Point out each leukocyte.
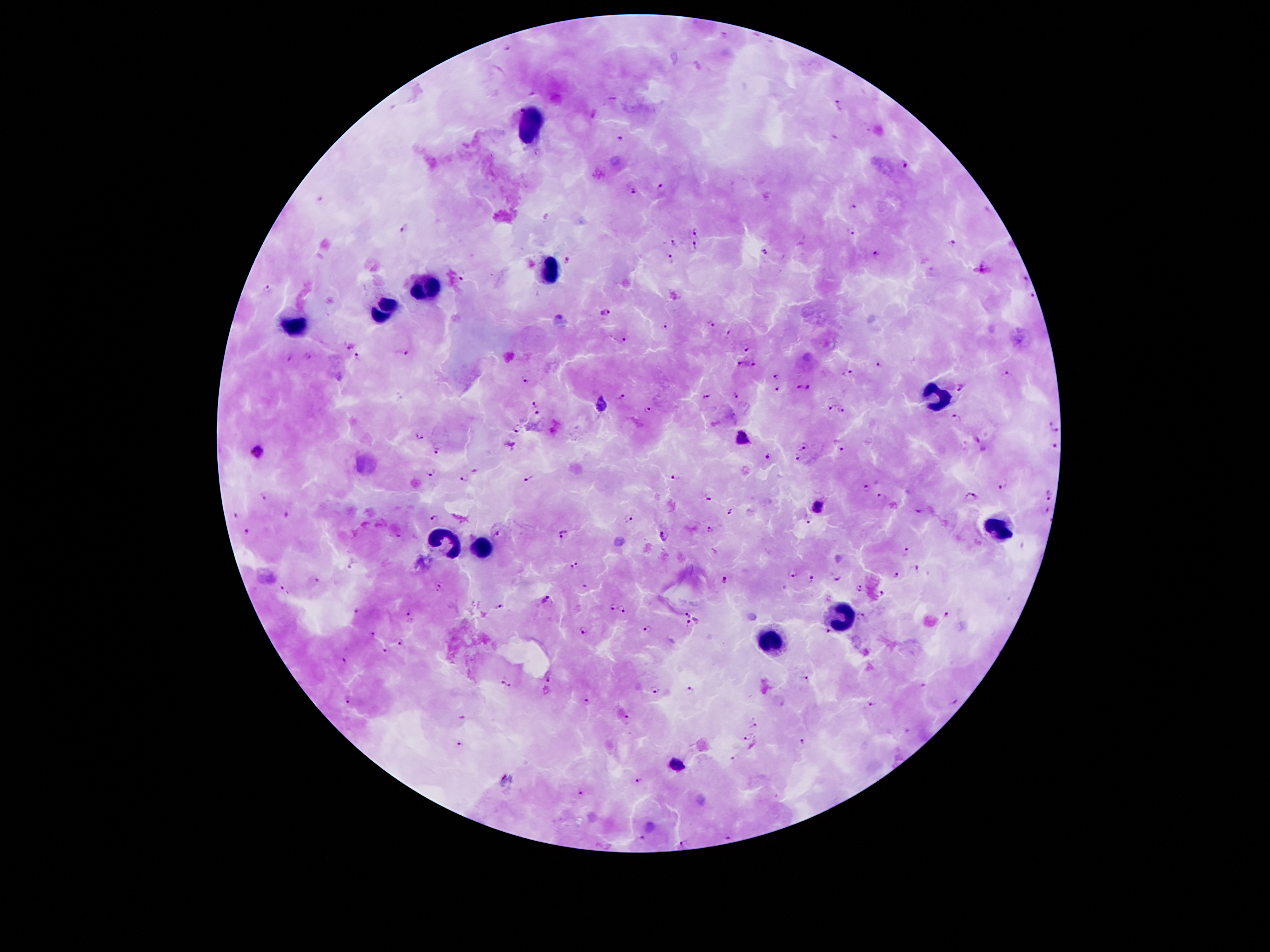

Approximate centers as (x, y) in pixels.
Leukocytes: (528, 120), (547, 269), (428, 286), (385, 309), (293, 327), (938, 394), (1001, 530), (447, 543), (483, 547), (842, 617), (771, 643).

Summary:
  - Malaria parasite locations: (722, 36), (504, 46), (532, 93), (840, 105), (518, 109), (594, 113), (621, 137), (905, 164), (658, 185), (632, 190), (321, 199), (854, 208), (406, 228), (697, 232), (851, 234), (671, 243), (950, 243), (694, 244), (764, 254), (876, 255), (669, 258), (568, 261), (982, 268), (463, 279), (1025, 280), (266, 288), (1030, 295), (603, 313), (711, 324), (667, 328), (730, 332), (623, 339), (346, 343), (747, 347), (404, 353), (289, 356), (358, 357), (304, 358), (741, 363), (879, 364), (753, 365), (847, 373), (1007, 375), (776, 377), (527, 378), (960, 386), (777, 387), (798, 387), (809, 387), (735, 396), (622, 397), (707, 398), (534, 402), (602, 406), (829, 406), (646, 407), (843, 410), (537, 411), (957, 416), (1050, 422), (517, 430), (1055, 431), (420, 437), (978, 438), (741, 440), (965, 444), (806, 445), (509, 447), (842, 447), (1054, 447), (437, 451), (260, 454), (767, 456), (798, 458), (476, 470), (430, 472), (528, 479), (462, 480), (675, 480), (1002, 484), (867, 488), (1049, 495), (263, 496), (880, 496), (970, 497), (706, 499), (819, 508), (919, 510), (1043, 510), (730, 511), (234, 514), (287, 514), (627, 516), (434, 518), (809, 520), (707, 529), (245, 530), (495, 533), (562, 534), (664, 535), (905, 551), (574, 565), (351, 567), (916, 568), (792, 575), (836, 575), (896, 575), (812, 576), (319, 578), (725, 579), (584, 585), (438, 589), (860, 589), (286, 590), (883, 594), (544, 600), (611, 605), (500, 606), (623, 607), (355, 610), (409, 610), (947, 614), (687, 615), (863, 617), (697, 621), (689, 624), (585, 629), (647, 629), (372, 633), (827, 633), (401, 642), (386, 650), (343, 661), (502, 679), (547, 679), (806, 679), (922, 685), (509, 686), (653, 689), (690, 689), (348, 698), (955, 699), (586, 702), (871, 704), (626, 716), (460, 718), (753, 723), (908, 730), (750, 737), (803, 741), (459, 743), (734, 760), (675, 765), (639, 780), (581, 793), (643, 836), (728, 836), (683, 841)
  - Stain: Giemsa
  - Image size: 1270×952 pixels
  - Patient malaria status: positive for Plasmodium falciparum
  - Capture: smartphone through the microscope eyepiece
  - Magnification: 100x
  - Preparation: thick peripheral-blood smear
  - Field of view: single